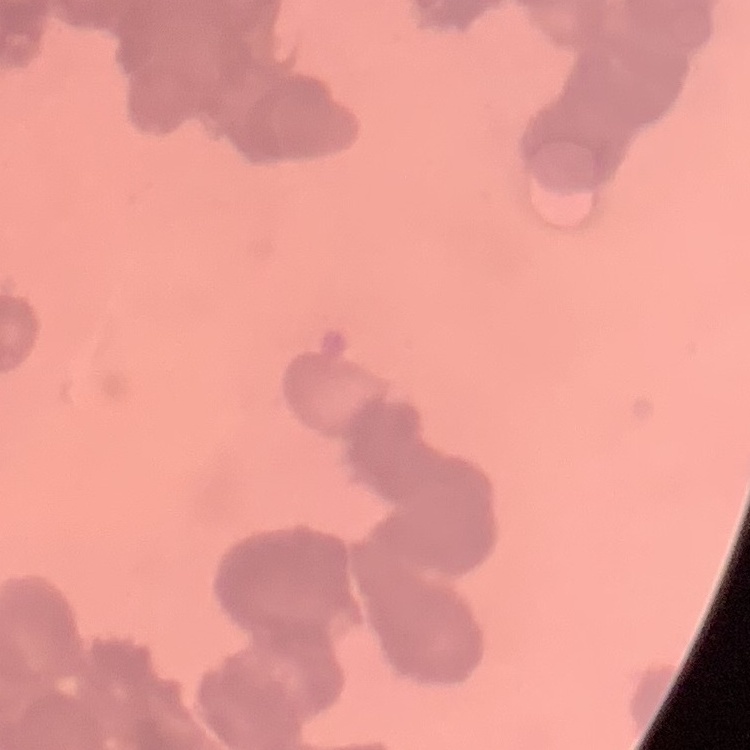
Summary:
  - Erythrocyte morphology: rouleaux formation
  - Stain: Field's or Giemsa
  - Image type: square crop of a larger photomicrograph
  - Preparation: thin peripheral smear